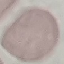

result = negative for malaria parasites
image type = automatically extracted cell patch, resized to 64 × 64 pixels
preparation = thin blood smear
capture = smartphone camera at the microscope eyepiece
stain = Giemsa